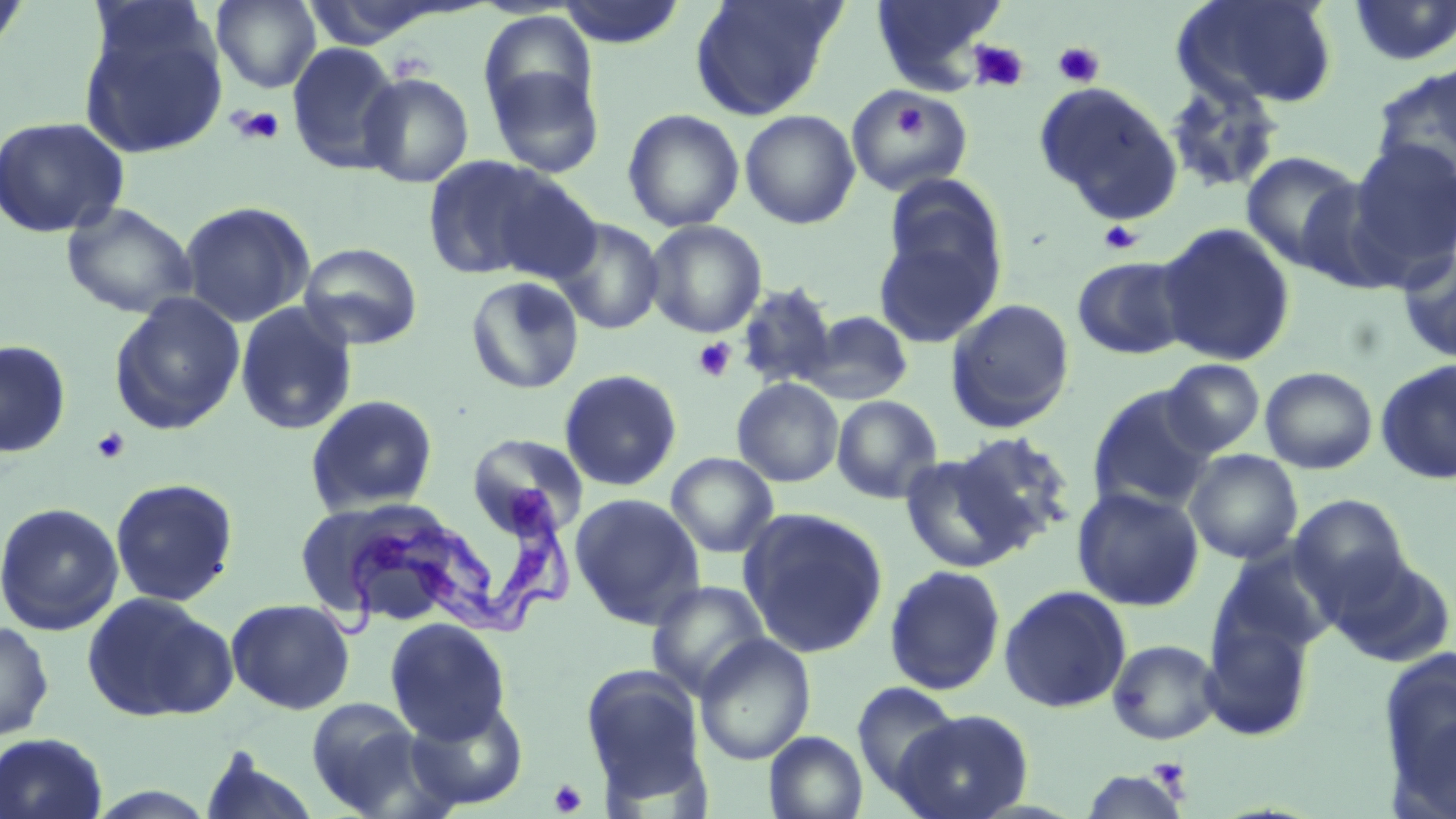

Summary:
  - Coordinate format: approximate bounding boxes as [x1, y1, x2, y2] in pixels
  - Trypanosoma brucei locations: [304, 483, 582, 644]
  - Platelet locations: [969, 40, 1030, 92], [1052, 41, 1105, 88], [890, 97, 928, 145], [229, 105, 286, 147], [1098, 220, 1143, 255], [693, 337, 736, 382], [91, 427, 130, 464], [1149, 759, 1191, 793], [549, 778, 587, 816]
  - Uninfected red blood cell locations: [0, 0, 32, 57], [211, 0, 322, 92], [555, 0, 687, 48], [689, 0, 844, 120], [870, 0, 1008, 91], [1172, 0, 1339, 111], [1347, 0, 1456, 66], [78, 15, 228, 160], [287, 41, 402, 175], [484, 58, 605, 178], [1369, 63, 1456, 189], [357, 71, 475, 188], [1163, 79, 1284, 195], [1034, 82, 1182, 223], [844, 86, 973, 196], [623, 108, 745, 231], [740, 109, 861, 230], [0, 116, 130, 238], [1348, 140, 1456, 279], [1240, 151, 1367, 273], [421, 155, 570, 282], [481, 170, 603, 283], [880, 173, 1008, 307], [60, 201, 198, 319], [179, 201, 315, 327], [552, 217, 665, 334], [645, 220, 767, 337], [872, 221, 1002, 350], [1156, 222, 1296, 367], [297, 242, 423, 350], [1398, 248, 1456, 363], [1071, 255, 1193, 360], [465, 276, 584, 394], [734, 282, 840, 390], [108, 292, 246, 436], [946, 298, 1076, 434], [234, 301, 359, 436], [800, 309, 914, 406], [0, 339, 72, 459], [1160, 358, 1266, 457], [1375, 358, 1456, 484], [1260, 366, 1378, 474], [558, 369, 683, 492], [732, 378, 844, 487], [1086, 385, 1218, 514], [305, 394, 439, 515], [832, 395, 943, 503], [950, 431, 1076, 550], [468, 433, 588, 536], [1184, 449, 1303, 564], [898, 451, 1029, 573], [665, 452, 779, 558], [110, 477, 239, 607], [1071, 485, 1204, 611], [570, 493, 706, 628], [1288, 494, 1412, 609], [304, 501, 484, 631], [0, 502, 124, 636], [738, 507, 889, 658], [1210, 550, 1337, 664], [1323, 550, 1455, 666], [884, 564, 1007, 695], [646, 580, 771, 699], [998, 584, 1132, 713], [81, 590, 237, 723], [226, 598, 356, 715], [1200, 611, 1316, 743], [384, 617, 511, 744], [0, 619, 55, 742], [695, 635, 815, 766], [1107, 638, 1222, 745], [1376, 644, 1456, 811], [579, 663, 710, 803], [851, 681, 961, 799], [304, 697, 430, 815], [405, 697, 530, 810], [894, 708, 1034, 819], [764, 731, 868, 819], [0, 732, 109, 819], [197, 750, 323, 819], [1080, 768, 1192, 818]
  - Slide-level diagnosis: Trypanosoma brucei
  - Image size: 1456×819 pixels
  - Field of view: one of a larger specimen
  - Preparation: thin blood smear
  - Modality: optical microscopy
  - Magnification: 1000x
  - Stain: May-Grünwald-Giemsa